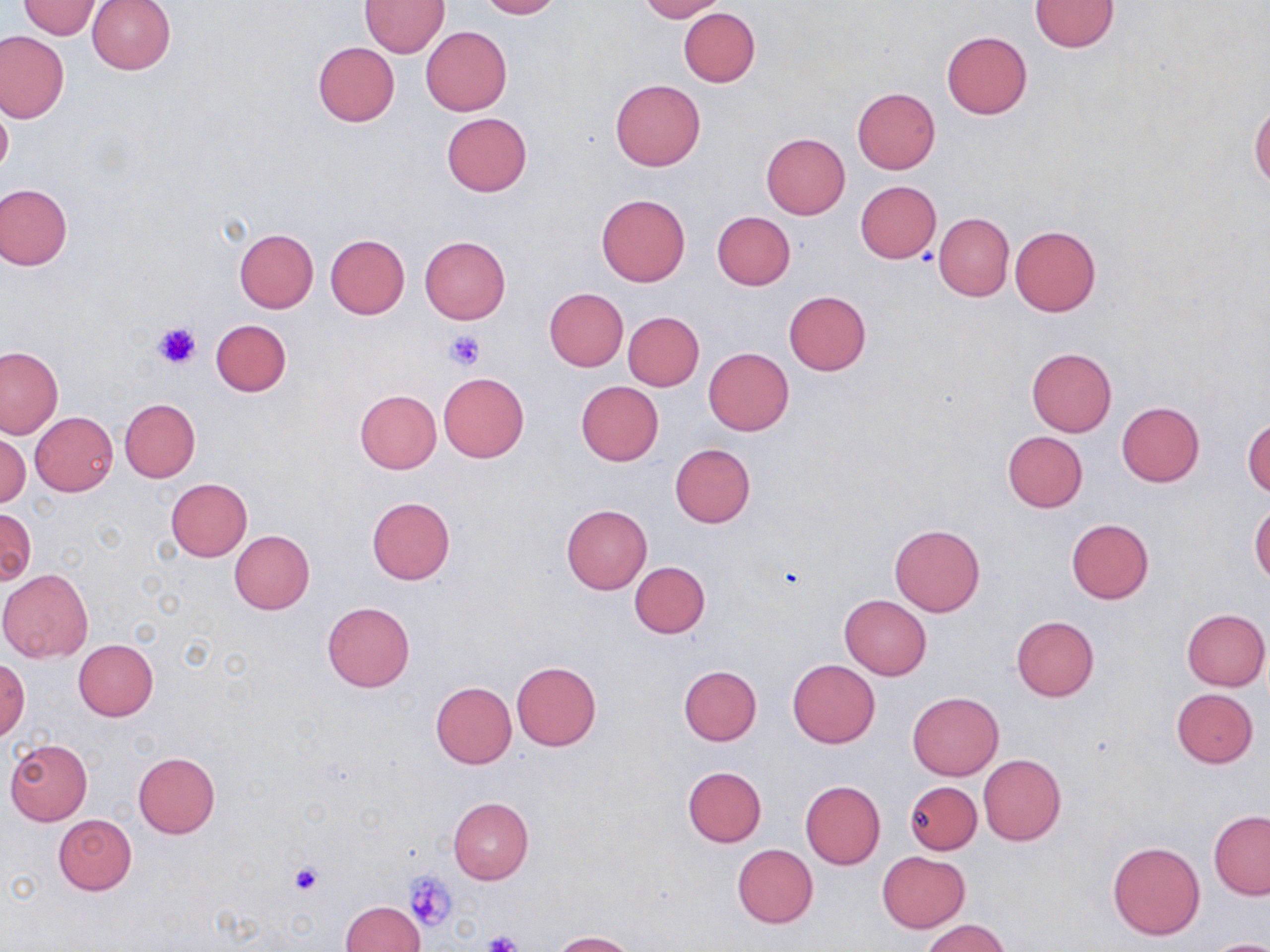
Approximate bounding boxes as [x1, y1, x2, y2] in pixels. Uninfected red blood cell locations: [87, 0, 175, 74], [360, 0, 448, 56], [476, 0, 560, 19], [639, 0, 725, 21], [1029, 0, 1118, 52], [19, 1, 101, 38], [678, 7, 760, 86], [421, 26, 511, 115], [942, 31, 1032, 119], [0, 32, 68, 121], [312, 41, 400, 126], [610, 80, 705, 171], [852, 87, 940, 174], [0, 101, 12, 183], [1249, 102, 1269, 190], [441, 113, 532, 196], [761, 133, 850, 219], [855, 180, 941, 262], [1, 184, 73, 270], [597, 194, 690, 286], [711, 211, 795, 289], [934, 212, 1013, 302], [1009, 224, 1100, 316], [233, 227, 318, 312], [325, 235, 410, 319], [419, 236, 510, 324], [544, 288, 629, 371], [783, 290, 871, 375], [624, 312, 703, 390], [210, 320, 291, 397], [0, 347, 64, 439], [703, 347, 795, 436], [1026, 347, 1117, 437], [439, 372, 529, 462], [575, 381, 664, 465], [355, 390, 441, 473], [120, 399, 200, 482], [1117, 401, 1205, 486], [29, 411, 118, 497], [1244, 416, 1269, 497], [1002, 431, 1088, 512], [0, 433, 30, 509], [669, 444, 755, 528], [166, 479, 252, 562], [366, 497, 456, 584], [1250, 500, 1269, 586], [561, 505, 651, 595], [2, 509, 35, 584], [1065, 519, 1154, 604], [889, 524, 985, 616], [230, 530, 315, 613], [630, 561, 710, 637], [0, 568, 92, 663], [839, 595, 931, 680], [322, 601, 415, 692], [1183, 609, 1269, 690], [1011, 616, 1099, 701], [73, 639, 158, 720], [787, 659, 879, 747], [0, 660, 29, 741], [510, 661, 603, 751], [677, 664, 762, 746], [430, 682, 516, 769], [1171, 688, 1258, 767], [908, 691, 1003, 780], [5, 738, 92, 825], [133, 752, 220, 837], [978, 753, 1065, 846], [683, 766, 767, 847], [801, 781, 886, 868], [905, 781, 981, 854], [447, 797, 534, 883], [1209, 810, 1270, 899], [52, 814, 138, 895], [1108, 840, 1204, 939], [732, 845, 818, 927], [878, 851, 969, 932], [340, 900, 425, 952], [920, 918, 1009, 952], [551, 930, 637, 952], [1203, 937, 1270, 952]. Platelet locations: [153, 320, 202, 369], [444, 330, 485, 371], [287, 861, 323, 896], [406, 871, 457, 932], [482, 932, 526, 952]. Slide-level diagnosis: negative for blood parasites. May-Grünwald-Giemsa stain. Thin blood smear. 1000x magnification. Image is 1270×952 pixels. Optical microscopy. One field of a larger specimen.